State the blood parasite species.
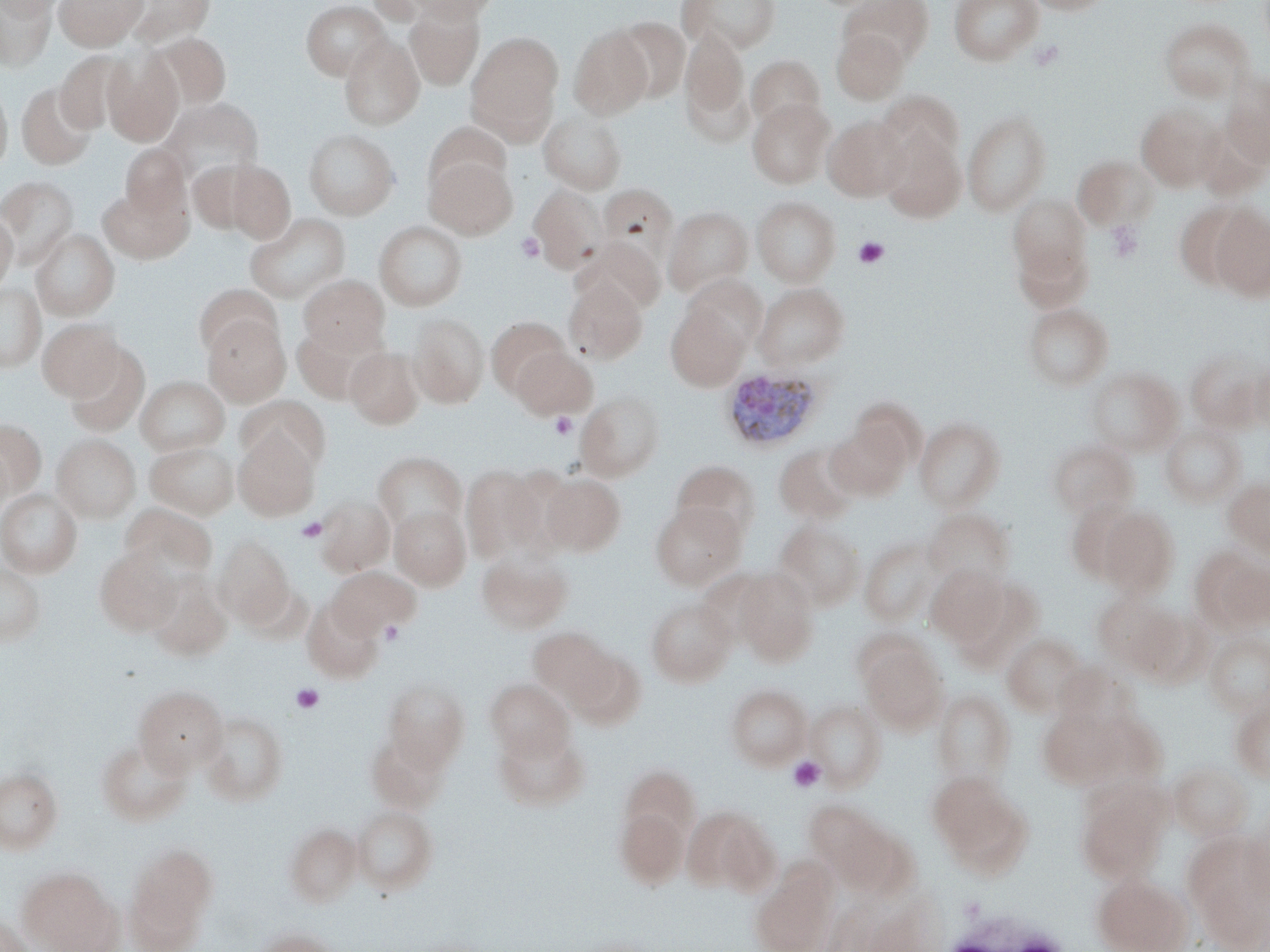
Plasmodium ovale.

Summary:
  - Coordinate format: approximate bounding boxes as (x1,y1)-(x2,y2) corner pairs in pixels
  - Uninfected red blood cell locations: (0,0)-(56,72), (1,0)-(64,18), (53,0)-(148,50), (124,0)-(214,47), (406,0)-(498,24), (678,0)-(781,53), (840,0)-(934,67), (948,0)-(1043,65), (1023,0)-(1112,15), (301,1)-(390,80), (405,3)-(484,88), (612,16)-(690,104), (1159,18)-(1253,102), (568,25)-(654,119), (681,27)-(749,131), (831,28)-(908,104), (150,33)-(232,109), (465,33)-(562,141), (339,35)-(424,129), (56,51)-(132,134), (102,51)-(183,146), (746,56)-(825,132), (1222,74)-(1270,168), (0,81)-(12,175), (17,82)-(97,170), (878,92)-(965,170), (161,98)-(263,185), (747,99)-(835,188), (1135,105)-(1224,191), (963,110)-(1051,216), (538,111)-(627,194), (822,115)-(911,201), (424,123)-(512,197), (304,129)-(399,219), (880,129)-(966,222), (120,144)-(190,223), (424,155)-(516,238), (1073,156)-(1159,230), (187,160)-(261,234), (226,161)-(295,243), (0,176)-(78,266), (599,183)-(679,263), (529,185)-(607,273), (98,186)-(190,263), (1008,194)-(1091,286), (752,197)-(840,286), (1173,202)-(1253,291), (663,207)-(752,296), (1209,207)-(1270,302), (0,211)-(18,293), (245,212)-(350,304), (374,221)-(467,310), (30,229)-(119,320), (574,238)-(666,314), (1013,239)-(1092,314), (298,275)-(389,354), (563,277)-(647,364), (683,277)-(767,354), (0,283)-(45,372), (754,283)-(848,369), (194,284)-(282,359), (1023,303)-(1113,390), (666,306)-(749,391), (409,312)-(489,407), (202,315)-(290,406), (486,317)-(572,399), (37,318)-(123,400), (292,324)-(377,404), (64,343)-(150,438), (345,347)-(424,429), (511,347)-(597,419), (1185,348)-(1264,431), (1248,364)-(1270,431), (1085,367)-(1182,455), (136,376)-(229,455), (576,391)-(665,481), (237,396)-(330,474), (850,397)-(925,471), (914,417)-(1005,512), (0,419)-(46,498), (826,423)-(909,501), (1160,423)-(1246,506), (234,431)-(320,521), (52,434)-(141,523), (1048,440)-(1137,517), (145,441)-(239,519), (774,443)-(860,524), (0,446)-(15,521), (373,452)-(466,535), (671,460)-(760,542), (460,465)-(547,563), (540,474)-(625,555), (1224,478)-(1270,556), (0,488)-(83,578), (315,496)-(395,576), (1066,499)-(1143,583), (650,502)-(745,590), (121,504)-(217,581), (389,506)-(470,590), (1098,507)-(1181,600), (924,508)-(1016,587), (775,521)-(865,610), (214,535)-(294,627), (860,537)-(941,625), (95,547)-(180,636), (476,548)-(573,634), (1201,552)-(1270,632), (0,563)-(46,645), (926,565)-(1007,645), (328,566)-(419,639), (734,569)-(819,665), (145,573)-(232,661), (948,573)-(1044,670), (1093,593)-(1181,672), (301,597)-(385,683), (646,597)-(736,686), (1125,610)-(1210,687), (529,627)-(615,711), (1204,632)-(1270,716), (1003,633)-(1087,716), (859,641)-(948,733), (566,648)-(646,730), (383,677)-(469,771), (485,679)-(574,759), (134,684)-(227,775), (726,684)-(812,769), (933,690)-(1016,787), (805,700)-(886,789), (1231,700)-(1270,782), (1038,707)-(1121,787), (200,711)-(288,806), (494,724)-(589,810), (366,732)-(451,813), (96,738)-(191,826), (1169,763)-(1251,840), (619,764)-(700,849), (0,768)-(62,853), (930,774)-(1031,874), (1075,779)-(1172,884), (351,805)-(438,894), (615,806)-(689,889), (682,806)-(776,895), (816,807)-(898,886), (1241,816)-(1270,903), (284,823)-(362,906), (1185,834)-(1269,943), (125,842)-(218,944), (751,865)-(836,952), (19,866)-(122,952), (1092,874)-(1190,952), (0,914)-(34,952), (251,928)-(340,952)
  - Plasmodium ovale-infected red blood cell locations: (718,367)-(826,452)
  - Platelet locations: (1105,221)-(1143,262), (516,233)-(545,263), (853,236)-(890,269), (549,412)-(577,439), (296,517)-(327,542), (380,620)-(405,646), (290,683)-(324,713), (788,756)-(826,792)
  - Preparation: thin blood film
  - Image size: 1270×952 pixels
  - Modality: optical microscopy
  - Field of view: one of a larger specimen
  - Magnification: 1000x
  - Stain: May-Grünwald-Giemsa